Locate every Plasmodium parasite and every leukocyte.
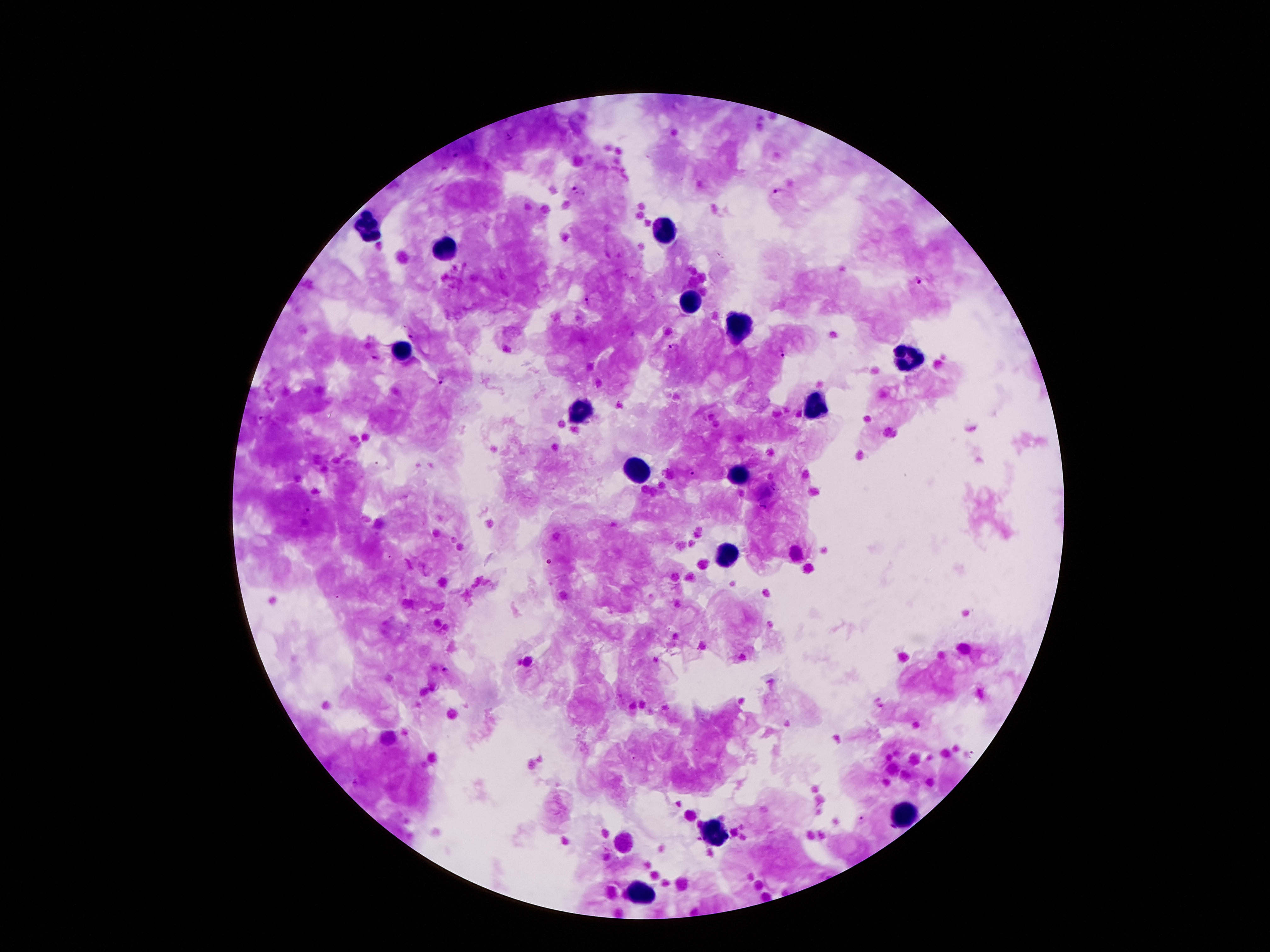

Approximate centers as {x, y} in pixels.
Plasmodium parasites: {509, 137}, {457, 156}, {578, 190}, {776, 192}, {919, 281}, {586, 298}, {411, 336}, {674, 348}, {780, 354}, {375, 356}, {440, 380}, {263, 419}, {689, 472}, {307, 510}, {444, 670}, {859, 819}.
Leukocytes: {367, 228}, {665, 232}, {443, 249}, {684, 302}, {737, 329}, {403, 352}, {913, 359}, {814, 407}, {581, 415}, {638, 468}, {737, 474}, {728, 556}, {903, 814}, {714, 835}, {640, 894}.

Summary:
  - Preparation: thick peripheral-blood smear
  - Field of view: single
  - Capture: smartphone through the microscope eyepiece
  - Patient malaria status: positive for Plasmodium falciparum
  - Magnification: 100x
  - Stain: Giemsa
  - Image size: 1270×952 pixels